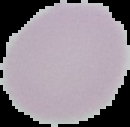
result = no Plasmodium parasites seen
image type = segmented cell region with the area outside set to black
image size = 130×127 pixels
preparation = thin blood film